Describe the morphology of the red blood cells.
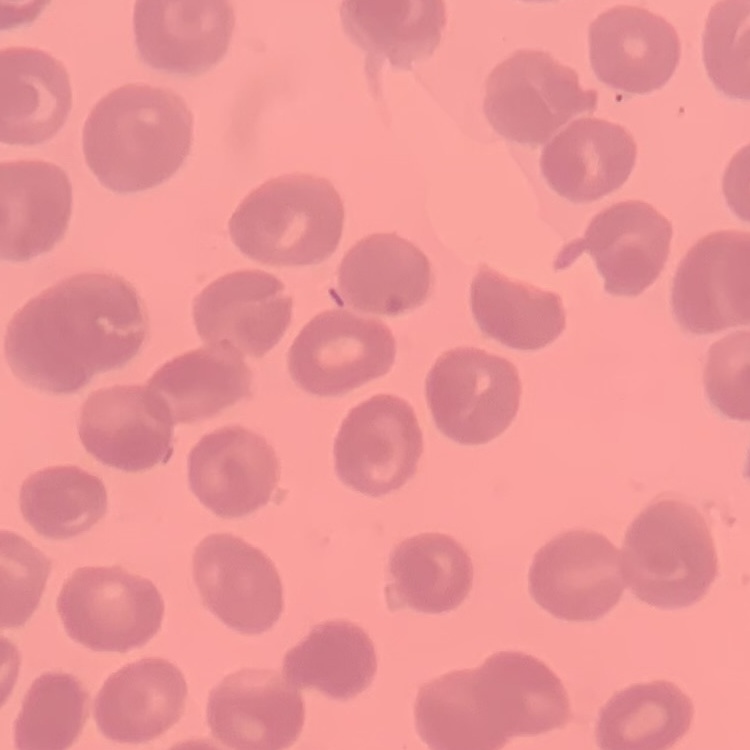

They show no rouleaux formation.

stain = Field's or Giemsa
image type = one tile cut from a larger photomicrograph
preparation = thin peripheral smear